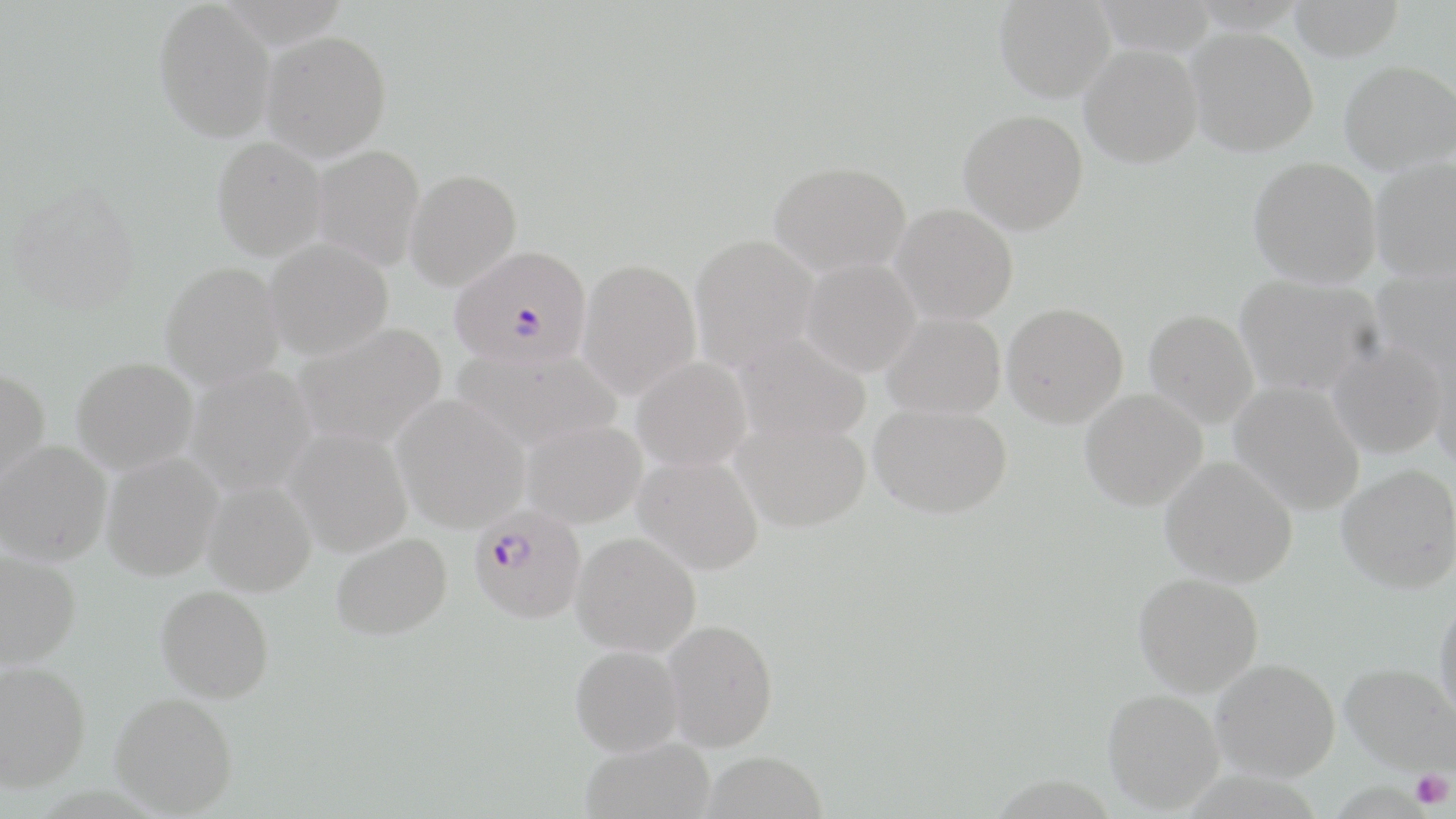
Summary:
  - Coordinate format: approximate bounding boxes as [x1, y1, x2, y2] in pixels
  - Platelet locations: [1410, 769, 1453, 810]
  - Plasmodium falciparum-infected red blood cell locations: [449, 245, 592, 369], [469, 505, 586, 624]
  - Uninfected red blood cell locations: [153, 0, 276, 142], [994, 0, 1115, 101], [1288, 0, 1404, 61], [1186, 27, 1317, 156], [261, 29, 392, 161], [1080, 44, 1202, 167], [1339, 60, 1456, 173], [958, 109, 1088, 234], [211, 136, 327, 260], [311, 145, 425, 270], [1248, 157, 1382, 287], [1370, 158, 1456, 282], [769, 160, 911, 275], [405, 169, 522, 291], [6, 181, 141, 315], [891, 204, 1018, 323], [690, 235, 819, 370], [264, 238, 394, 359], [577, 258, 701, 400], [800, 259, 920, 377], [160, 262, 285, 389], [1369, 265, 1456, 384], [1235, 274, 1384, 397], [1002, 303, 1128, 427], [1144, 309, 1259, 427], [882, 312, 1006, 420], [292, 322, 448, 450], [732, 332, 871, 446], [1327, 338, 1447, 459], [1427, 345, 1456, 468], [452, 346, 623, 453], [631, 356, 752, 472], [71, 357, 198, 474], [186, 365, 317, 496], [0, 368, 50, 490], [1230, 381, 1365, 515], [1080, 389, 1207, 510], [392, 394, 529, 532], [870, 403, 1012, 518], [732, 416, 871, 532], [521, 419, 647, 528], [284, 427, 412, 557], [0, 441, 111, 566], [101, 453, 222, 581], [634, 454, 764, 574], [1160, 456, 1298, 587], [1337, 465, 1456, 593], [202, 479, 316, 597], [571, 532, 701, 657], [330, 533, 452, 641], [0, 550, 82, 668], [1133, 572, 1263, 696], [155, 585, 275, 703], [1434, 597, 1456, 725], [663, 619, 779, 751], [570, 644, 684, 756], [1211, 658, 1340, 781], [0, 660, 91, 791], [1341, 662, 1455, 778], [1103, 688, 1224, 812], [109, 692, 238, 816], [580, 736, 715, 819], [703, 750, 828, 819]
  - Slide-level diagnosis: Plasmodium falciparum
  - Modality: optical microscopy
  - Magnification: 1000x
  - Image size: 1456×819 pixels
  - Field of view: one of a larger specimen
  - Stain: May-Grünwald-Giemsa
  - Preparation: thin blood film